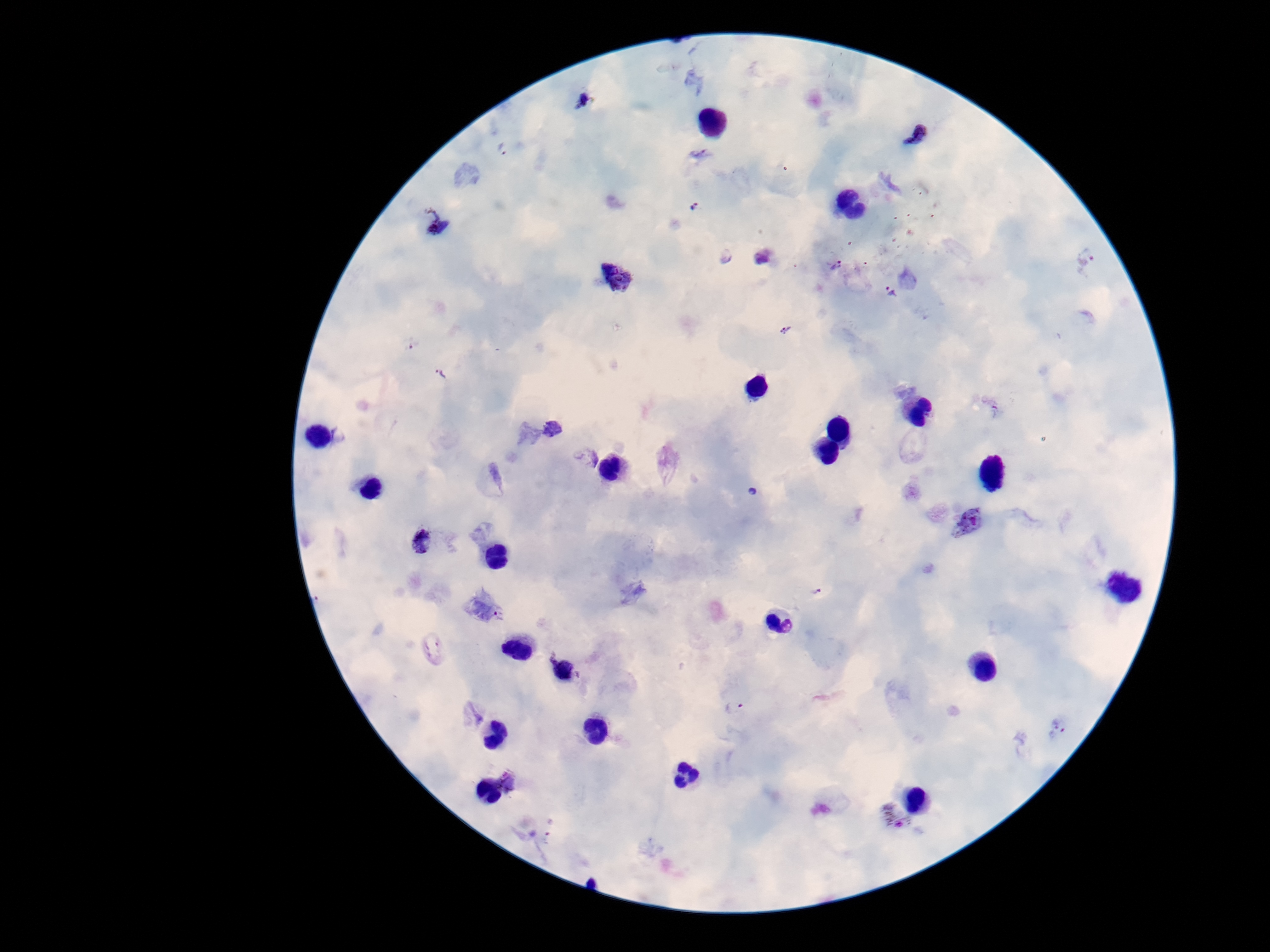
Approximate object centers, in pixels from the top-left corner.
Summary:
  - Plasmodium parasite locations: (x=583, y=100), (x=916, y=135), (x=502, y=150), (x=694, y=207), (x=435, y=222), (x=764, y=255), (x=727, y=257), (x=1088, y=262), (x=838, y=265), (x=617, y=279), (x=891, y=291), (x=785, y=331), (x=412, y=343), (x=441, y=373), (x=989, y=407), (x=553, y=428), (x=590, y=456), (x=970, y=522), (x=422, y=540), (x=815, y=592), (x=563, y=669), (x=735, y=708), (x=1058, y=727), (x=508, y=782), (x=893, y=819)
  - Preparation: thick peripheral-blood smear
  - Field of view: one from this slide
  - Image size: 1270×952 pixels
  - Patient malaria status: positive
  - Magnification: 100x
  - Capture: smartphone camera through the microscope eyepiece
  - Stain: Giemsa